Outline each blood parasite and name the species.
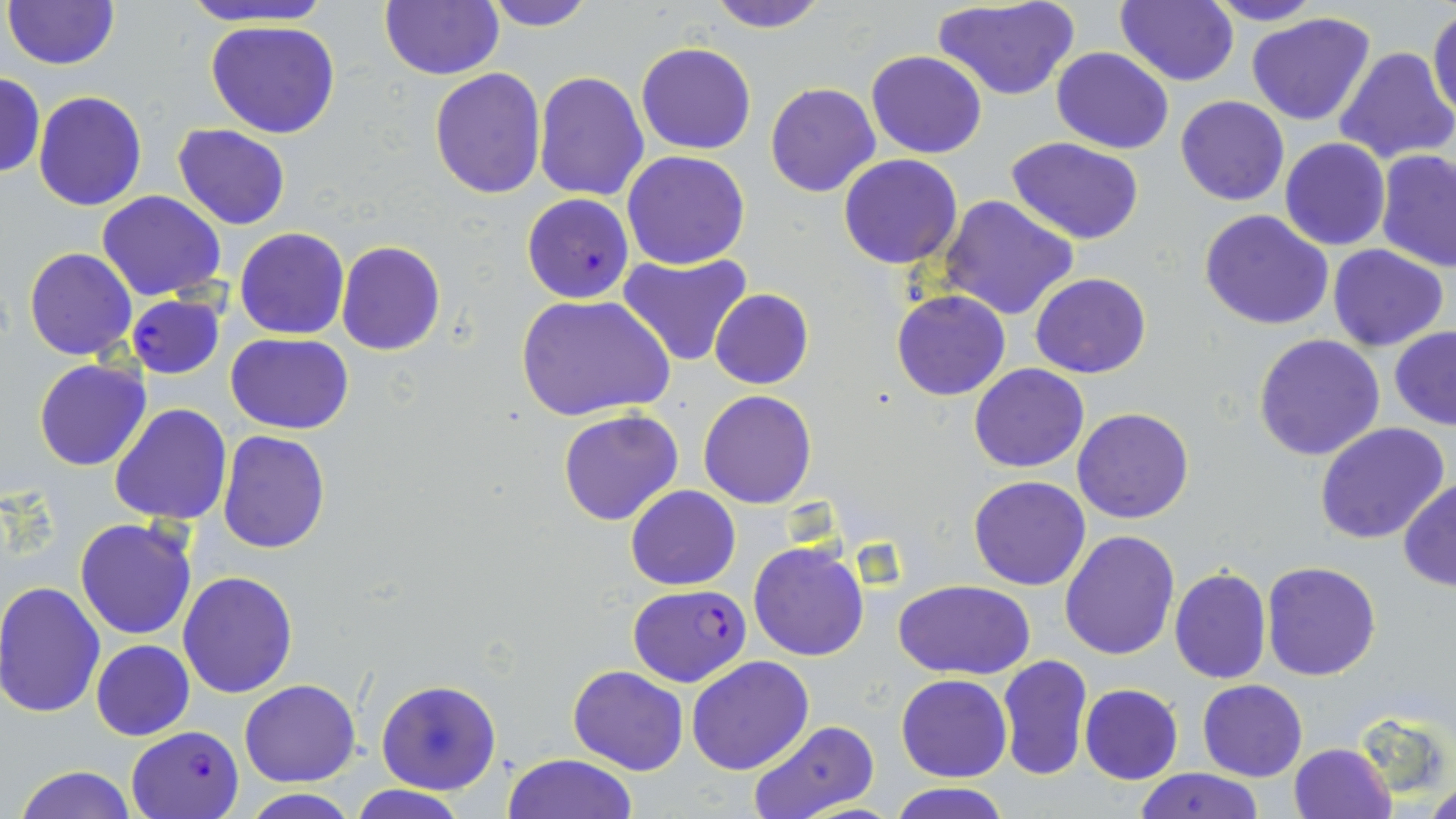

Approximate bounding boxes as (x1,y1)-(x2,y2) corner pairs in pixels.
Plasmodium falciparum-infected red blood cells: (521,194)-(635,304), (125,294)-(227,379), (626,584)-(751,686), (127,725)-(245,817).
No Plasmodium ovale, Plasmodium malariae, Plasmodium vivax, Babesia divergens, or Trypanosoma brucei observed.

slide-level diagnosis = Plasmodium falciparum
field of view = single
preparation = thin blood film
magnification = 1000x
image size = 1456×819 pixels
modality = light microscopy
uninfected red blood cell locations = approximate bounding boxes as (x1,y1)-(x2,y2) corner pairs in pixels: (182,0)-(333,29), (379,0)-(504,80), (479,0)-(601,30), (705,0)-(831,33), (1115,0)-(1238,86), (1200,0)-(1327,26), (5,1)-(120,71), (934,1)-(1079,101), (1429,6)-(1456,122), (1246,12)-(1378,126), (205,20)-(340,139), (636,42)-(756,155), (1052,46)-(1173,155), (1333,46)-(1455,166), (866,50)-(987,159), (428,67)-(546,198), (533,70)-(650,201), (0,71)-(45,178), (764,82)-(880,198), (31,92)-(147,211), (1176,95)-(1288,206), (172,125)-(293,230), (1006,136)-(1145,244), (1280,138)-(1390,252), (621,150)-(750,269), (1377,150)-(1456,274), (839,154)-(963,270), (97,190)-(226,303), (939,195)-(1079,321), (1199,209)-(1334,332), (234,226)-(349,341), (336,240)-(445,356), (1328,245)-(1448,350), (25,248)-(137,362), (618,252)-(750,368), (1030,273)-(1151,378), (710,288)-(814,391), (891,289)-(1010,402), (517,295)-(674,426), (1389,326)-(1456,430), (226,333)-(355,434), (1253,335)-(1385,460), (33,358)-(151,470), (969,363)-(1089,474), (699,390)-(817,510), (108,403)-(232,526), (1072,407)-(1194,525), (557,408)-(685,527), (1314,422)-(1450,543), (216,429)-(333,553), (968,475)-(1091,590), (1397,478)-(1456,593), (626,485)-(741,590), (75,518)-(200,640), (1060,531)-(1181,661), (748,541)-(870,662), (1260,560)-(1382,681), (1169,567)-(1271,684), (177,570)-(300,698), (895,579)-(1035,678), (0,582)-(106,720), (90,639)-(195,740), (996,654)-(1092,781), (685,656)-(815,775), (568,665)-(689,776), (896,674)-(1012,782), (376,678)-(502,796), (239,679)-(361,785), (1197,680)-(1307,782), (1080,683)-(1183,783), (745,720)-(880,819), (1288,743)-(1395,818), (502,753)-(640,818), (13,766)-(139,819), (1133,767)-(1265,819), (885,781)-(1014,818), (1419,782)-(1456,819), (347,784)-(471,819), (239,791)-(360,819)
stain = May-Grünwald-Giemsa